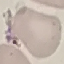
Result: negative for malaria parasites. Giemsa-stained preparation. Automatically extracted cell patch, resized to 64 × 64 pixels. Acquired by smartphone through the microscope eyepiece. Thin smear of blood.